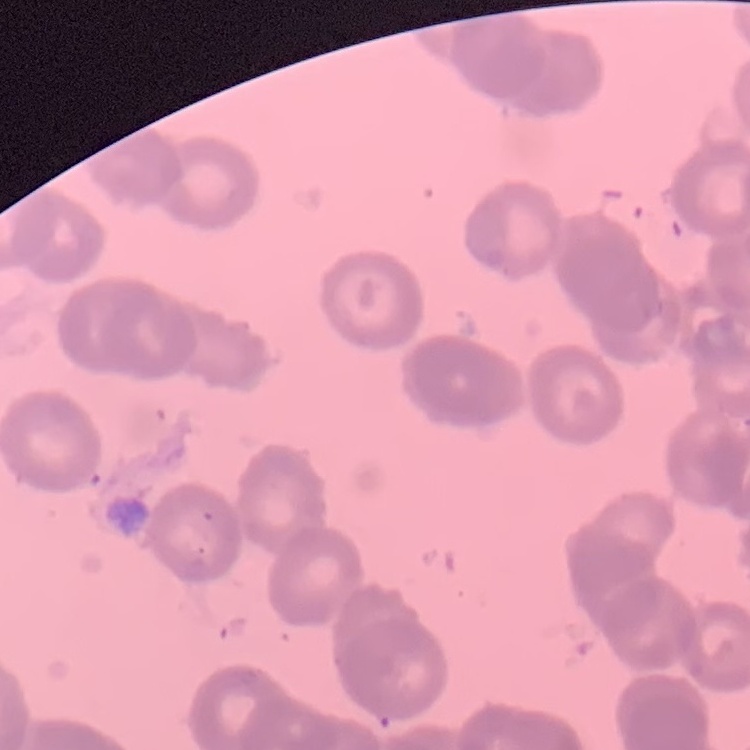
The red blood cells show rouleaux formation. Thin blood smear. Field's or Giemsa stain. One tile cut from a larger photomicrograph.